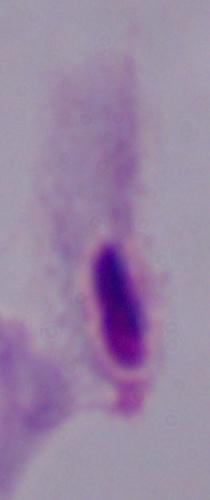

magnification: 1000x
modality: photomicrograph
identification: trichomonad